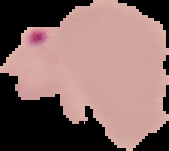
{
  "malaria_status": "uninfected",
  "preparation": "thin blood smear",
  "image_size": "169×151 pixels",
  "image_type": "cell region segmented out of the field of view; surrounding area masked to black"
}